Locate every malaria parasite by life-cycle stage, and every leukocyte.
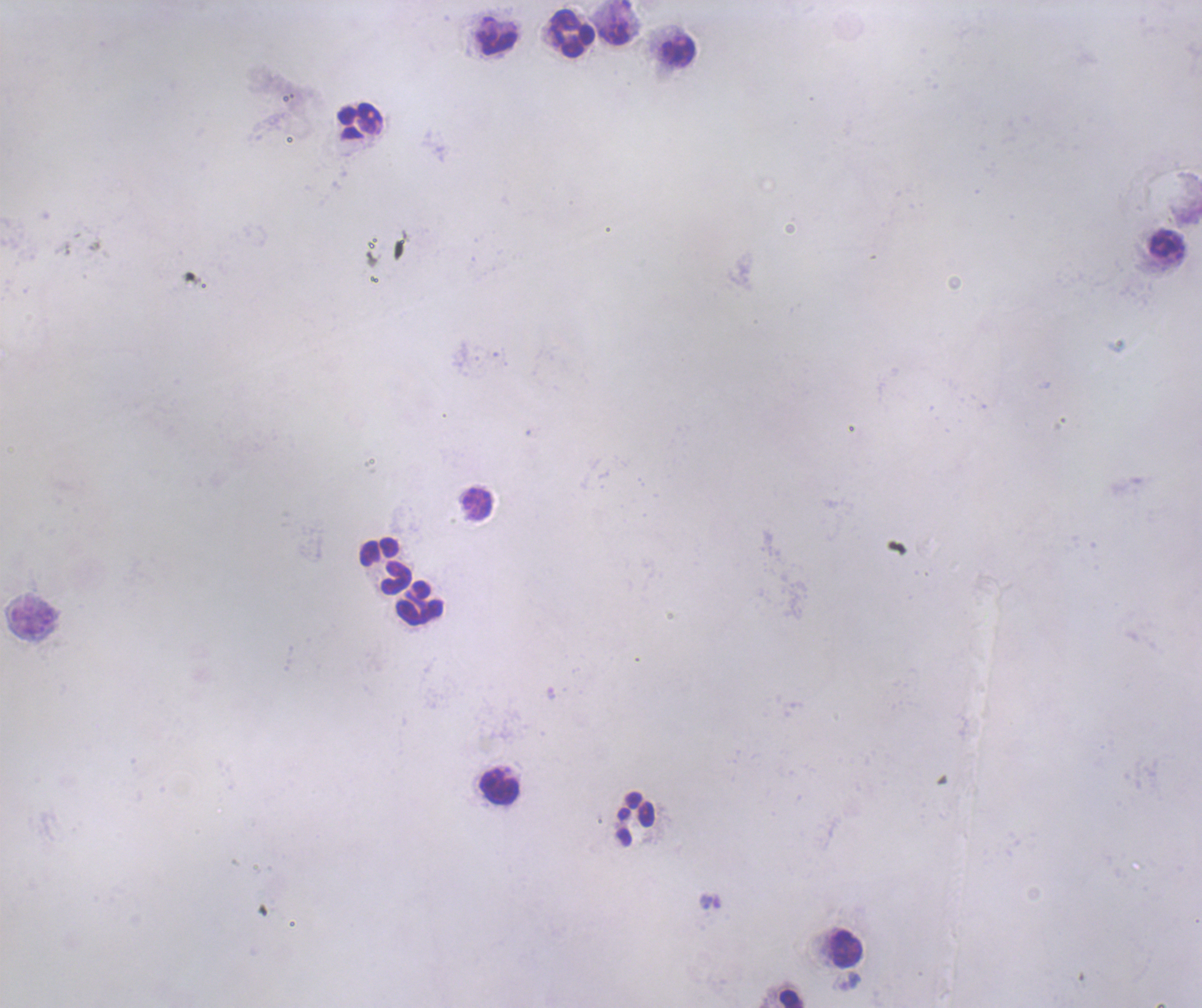
No malaria parasites seen.
Approximate centers as [x, y] in pixels.
Leukocytes: [572, 33], [496, 42], [678, 51], [360, 120], [477, 503], [386, 565], [420, 602], [498, 785], [635, 818], [847, 949].

Thick blood smear. Background quality: poor. Previously used in a real diagnosis. Coloration quality: bad. Romanowsky-stained preparation. Single field of view. Image is 1202×1008 pixels. 100x magnification.